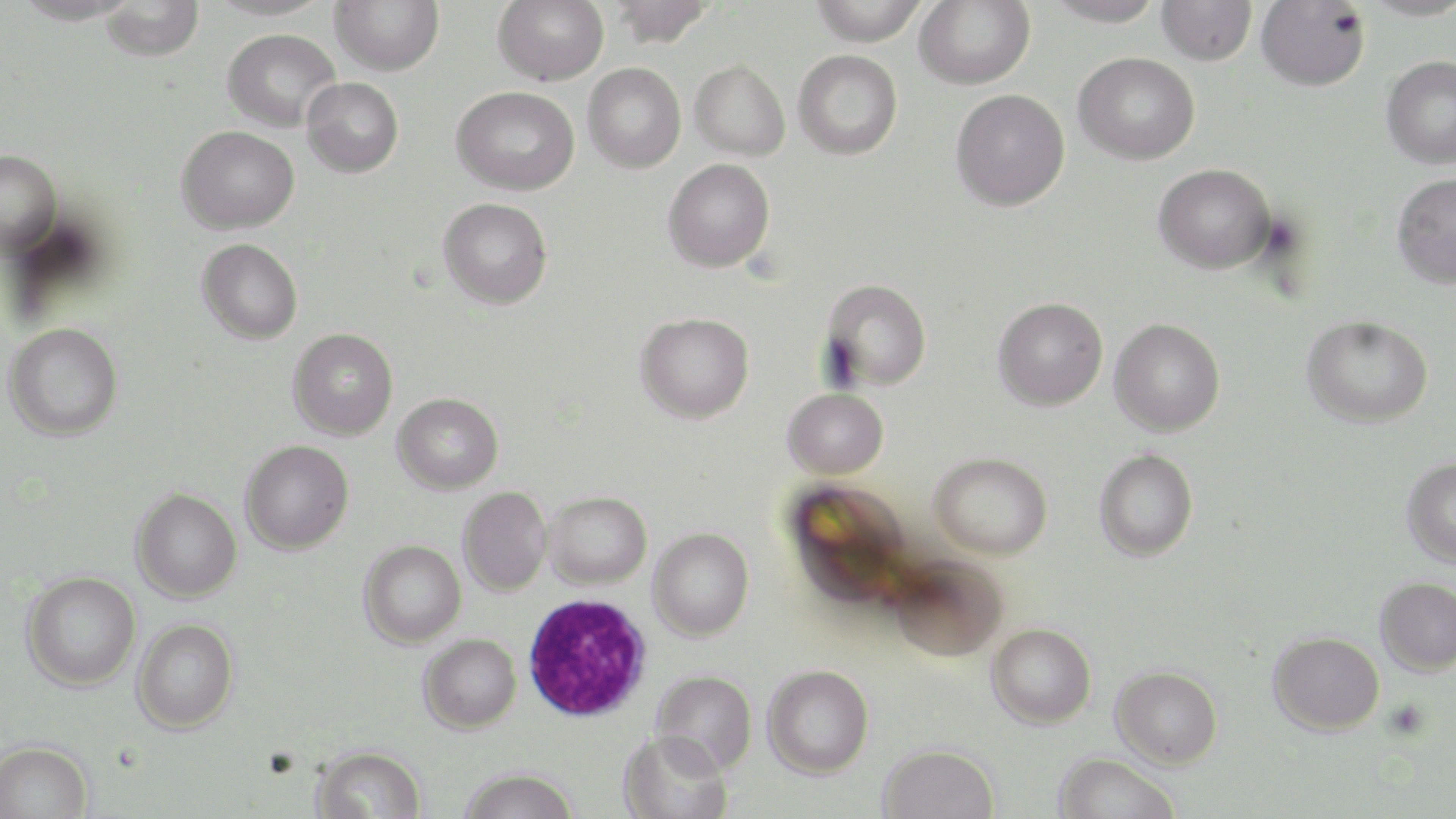

Summary:
  - Coordinate format: approximate bounding boxes as [x1, y1, x2, y2] in pixels
  - White blood cell locations: [522, 592, 652, 721]
  - Uninfected red blood cell locations: [205, 0, 333, 20], [330, 0, 444, 76], [493, 0, 609, 86], [608, 0, 716, 48], [809, 0, 929, 45], [915, 0, 1036, 89], [1044, 0, 1165, 27], [1359, 0, 1456, 20], [99, 1, 205, 62], [1157, 1, 1257, 65], [1256, 1, 1370, 90], [222, 28, 341, 132], [793, 49, 903, 160], [1073, 52, 1200, 165], [1381, 55, 1456, 169], [690, 59, 790, 160], [583, 63, 686, 173], [301, 77, 404, 178], [451, 85, 580, 196], [950, 89, 1070, 211], [176, 125, 299, 234], [0, 149, 61, 257], [663, 158, 775, 272], [1153, 163, 1276, 273], [1391, 172, 1456, 289], [438, 197, 552, 309], [197, 238, 303, 344], [821, 278, 932, 391], [992, 296, 1108, 411], [635, 312, 754, 423], [1300, 314, 1434, 428], [1109, 318, 1225, 437], [4, 323, 123, 441], [288, 327, 398, 440], [783, 387, 888, 479], [392, 392, 504, 494], [240, 440, 354, 554], [1094, 448, 1198, 562], [929, 452, 1052, 559], [1401, 457, 1456, 568], [783, 479, 915, 610], [458, 486, 552, 596], [131, 487, 242, 602], [543, 491, 651, 590], [648, 527, 754, 641], [359, 540, 466, 648], [887, 555, 1008, 662], [21, 571, 141, 690], [1375, 577, 1456, 677], [132, 617, 239, 733], [987, 622, 1096, 728], [1268, 630, 1385, 735], [418, 634, 521, 733], [762, 664, 874, 778], [1111, 665, 1223, 769], [651, 669, 757, 774], [618, 729, 733, 819], [0, 740, 93, 819], [878, 743, 999, 819], [312, 745, 426, 819], [1053, 752, 1182, 819], [457, 767, 579, 819]
  - Slide-level diagnosis: Plasmodium falciparum
  - Stain: May-Grünwald-Giemsa
  - Preparation: thin blood film
  - Magnification: 1000x
  - Modality: optical microscopy
  - Field of view: single
  - Image size: 1456×819 pixels